Locate platelets.
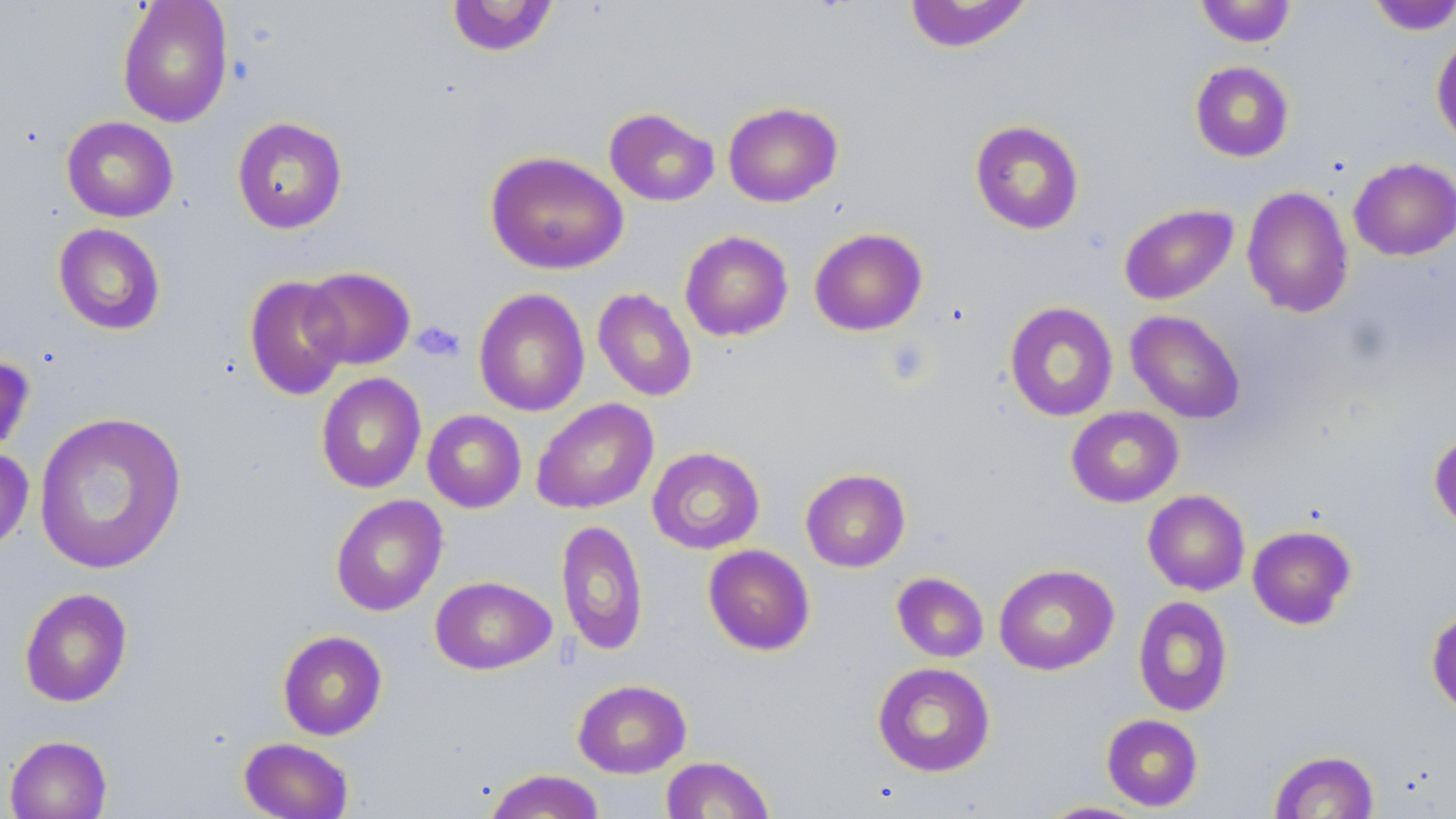

Approximate bounding boxes as named x1/y1/x2/y2 corners in pixels.
Platelets: (x1=412, y1=321, x2=465, y2=362).

Uninfected red blood cell locations: (x1=447, y1=0, x2=559, y2=57), (x1=1367, y1=0, x2=1456, y2=35), (x1=116, y1=1, x2=234, y2=128), (x1=903, y1=1, x2=1033, y2=53), (x1=1195, y1=1, x2=1297, y2=47), (x1=1431, y1=34, x2=1456, y2=147), (x1=1190, y1=61, x2=1294, y2=162), (x1=723, y1=101, x2=843, y2=207), (x1=604, y1=107, x2=720, y2=206), (x1=61, y1=116, x2=178, y2=222), (x1=232, y1=117, x2=347, y2=234), (x1=969, y1=119, x2=1084, y2=235), (x1=485, y1=150, x2=628, y2=275), (x1=1348, y1=157, x2=1456, y2=260), (x1=1242, y1=186, x2=1354, y2=318), (x1=1118, y1=204, x2=1238, y2=305), (x1=53, y1=223, x2=165, y2=335), (x1=809, y1=228, x2=928, y2=336), (x1=680, y1=230, x2=793, y2=342), (x1=301, y1=266, x2=415, y2=370), (x1=243, y1=275, x2=351, y2=400), (x1=473, y1=288, x2=590, y2=417), (x1=592, y1=288, x2=697, y2=402), (x1=1004, y1=302, x2=1118, y2=421), (x1=1126, y1=310, x2=1245, y2=424), (x1=0, y1=352, x2=36, y2=456), (x1=316, y1=372, x2=426, y2=493), (x1=532, y1=398, x2=658, y2=514), (x1=1066, y1=406, x2=1183, y2=508), (x1=422, y1=409, x2=526, y2=513), (x1=33, y1=411, x2=187, y2=575), (x1=1429, y1=431, x2=1456, y2=534), (x1=0, y1=446, x2=34, y2=556), (x1=647, y1=447, x2=765, y2=554), (x1=800, y1=468, x2=911, y2=572), (x1=1143, y1=490, x2=1250, y2=596), (x1=330, y1=494, x2=448, y2=617), (x1=555, y1=519, x2=649, y2=657), (x1=1247, y1=525, x2=1357, y2=629), (x1=703, y1=544, x2=815, y2=656), (x1=994, y1=564, x2=1119, y2=675), (x1=891, y1=572, x2=989, y2=662), (x1=430, y1=576, x2=556, y2=674), (x1=19, y1=587, x2=133, y2=708), (x1=1133, y1=596, x2=1233, y2=716), (x1=1426, y1=609, x2=1456, y2=716), (x1=277, y1=630, x2=387, y2=741), (x1=872, y1=662, x2=996, y2=777), (x1=572, y1=679, x2=691, y2=778), (x1=1101, y1=714, x2=1203, y2=812), (x1=4, y1=735, x2=113, y2=819), (x1=238, y1=737, x2=354, y2=819), (x1=1269, y1=750, x2=1379, y2=819), (x1=660, y1=755, x2=775, y2=818), (x1=484, y1=769, x2=605, y2=819), (x1=1036, y1=800, x2=1152, y2=818). Slide-level diagnosis: negative for blood parasites. Image is 1456×819 pixels. May-Grünwald-Giemsa-stained preparation. Thin blood smear. One field of a larger specimen. Captured at 1000x magnification. Light microscopy.